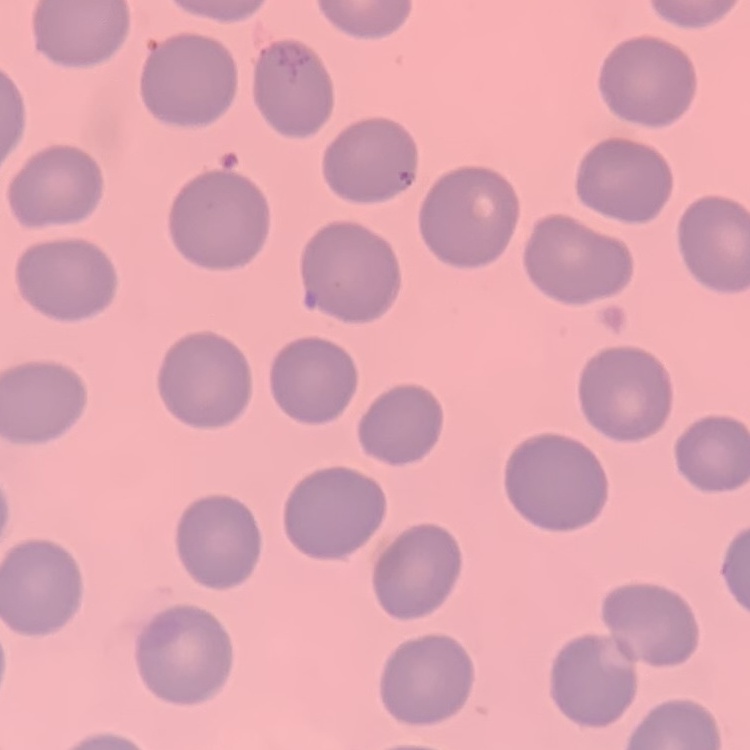
The erythrocytes show no rouleaux formation. Square crop of a larger photomicrograph. Field's or Giemsa stain. Thin peripheral smear.